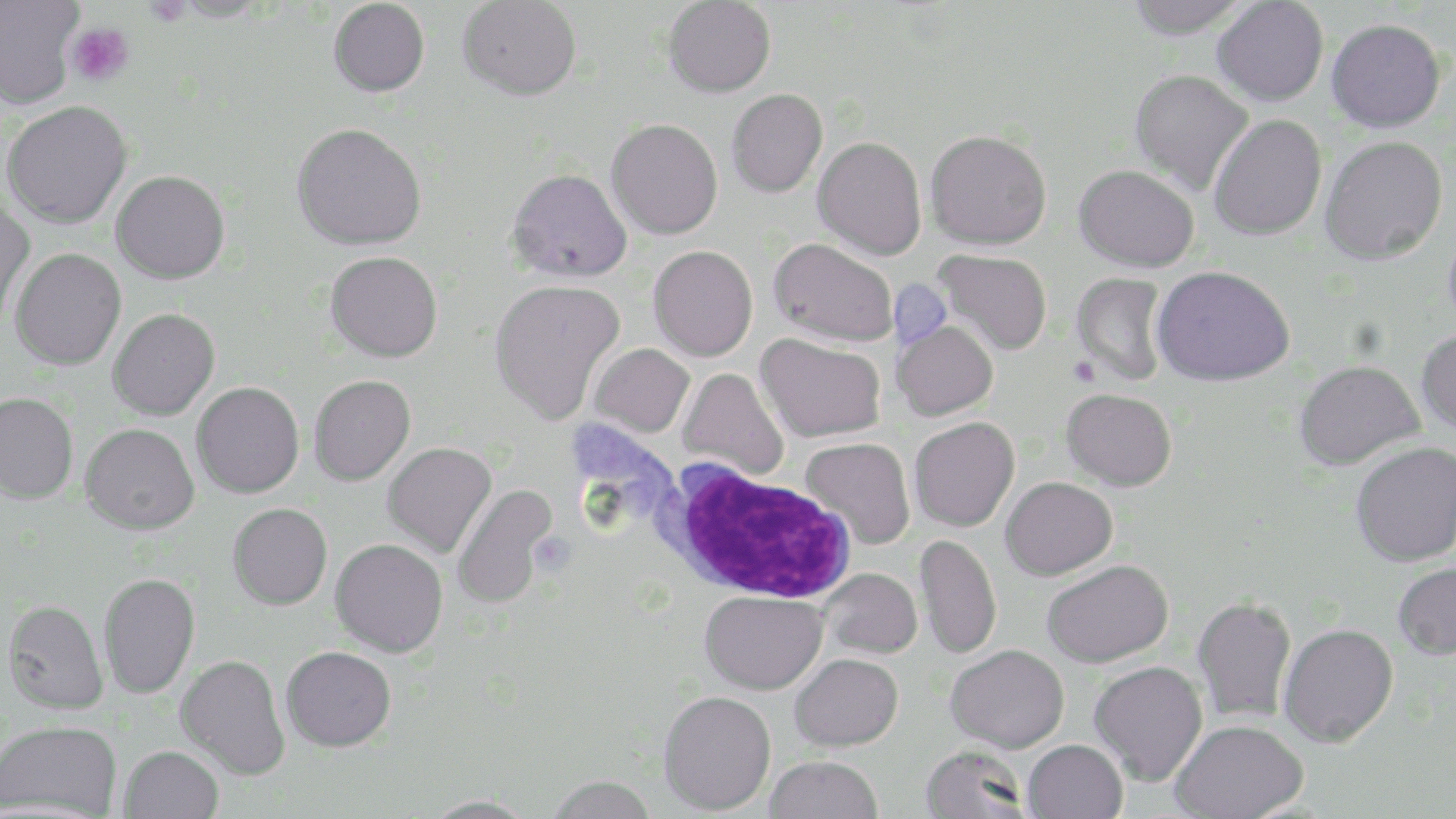
slide_level_diagnosis: Plasmodium falciparum
uninfected_red_blood_cell_locations: 'approximate bounding boxes as named x1/y1/x2/y2 corners in pixels: (x1=0, y1=0, x2=82, y2=109), (x1=167, y1=0, x2=274, y2=23), (x1=328, y1=0, x2=429, y2=97), (x1=458, y1=0, x2=581, y2=101), (x1=1125, y1=0, x2=1251, y2=39), (x1=663, y1=1, x2=776, y2=97), (x1=1212, y1=1, x2=1328, y2=106), (x1=1326, y1=18, x2=1445, y2=132), (x1=1130, y1=69, x2=1254, y2=195), (x1=726, y1=89, x2=827, y2=197), (x1=2, y1=101, x2=133, y2=228), (x1=1208, y1=114, x2=1327, y2=241), (x1=606, y1=118, x2=722, y2=239), (x1=291, y1=122, x2=426, y2=250), (x1=925, y1=129, x2=1052, y2=250), (x1=812, y1=136, x2=927, y2=260), (x1=1320, y1=136, x2=1448, y2=265), (x1=1074, y1=164, x2=1199, y2=272), (x1=507, y1=167, x2=632, y2=282), (x1=111, y1=170, x2=230, y2=284), (x1=0, y1=200, x2=35, y2=324), (x1=1443, y1=217, x2=1456, y2=337), (x1=769, y1=238, x2=897, y2=347), (x1=648, y1=245, x2=758, y2=361), (x1=10, y1=249, x2=126, y2=370), (x1=933, y1=249, x2=1052, y2=355), (x1=325, y1=251, x2=443, y2=362), (x1=1151, y1=265, x2=1295, y2=385), (x1=1070, y1=273, x2=1172, y2=386), (x1=489, y1=279, x2=625, y2=424), (x1=108, y1=308, x2=220, y2=420), (x1=892, y1=319, x2=998, y2=420), (x1=1417, y1=328, x2=1456, y2=435), (x1=756, y1=333, x2=886, y2=442), (x1=588, y1=343, x2=695, y2=437), (x1=1294, y1=360, x2=1424, y2=470), (x1=677, y1=368, x2=789, y2=481), (x1=309, y1=374, x2=415, y2=485), (x1=192, y1=381, x2=304, y2=498), (x1=1061, y1=388, x2=1177, y2=491), (x1=0, y1=392, x2=78, y2=504), (x1=909, y1=417, x2=1019, y2=531), (x1=80, y1=422, x2=199, y2=534), (x1=800, y1=437, x2=915, y2=548), (x1=382, y1=442, x2=497, y2=558), (x1=1351, y1=442, x2=1456, y2=567), (x1=1000, y1=476, x2=1117, y2=580), (x1=450, y1=484, x2=559, y2=609), (x1=228, y1=503, x2=332, y2=610), (x1=914, y1=534, x2=1002, y2=660), (x1=330, y1=538, x2=448, y2=657), (x1=1041, y1=560, x2=1173, y2=667), (x1=1392, y1=562, x2=1456, y2=660), (x1=819, y1=568, x2=922, y2=659), (x1=99, y1=573, x2=200, y2=698), (x1=699, y1=590, x2=827, y2=695), (x1=1192, y1=596, x2=1297, y2=724), (x1=3, y1=601, x2=108, y2=714), (x1=1278, y1=623, x2=1398, y2=747), (x1=945, y1=644, x2=1069, y2=753), (x1=281, y1=646, x2=396, y2=751), (x1=175, y1=654, x2=290, y2=779), (x1=789, y1=654, x2=903, y2=751), (x1=1089, y1=661, x2=1207, y2=785), (x1=658, y1=690, x2=776, y2=814), (x1=1171, y1=719, x2=1308, y2=819), (x1=0, y1=720, x2=121, y2=818), (x1=1022, y1=739, x2=1127, y2=818), (x1=920, y1=744, x2=1031, y2=818), (x1=120, y1=746, x2=223, y2=819), (x1=764, y1=755, x2=883, y2=818), (x1=544, y1=775, x2=659, y2=819), (x1=420, y1=795, x2=538, y2=819)'
field_of_view: one of a larger specimen
preparation: thin blood film
magnification: 1000x
modality: optical microscopy
stain: May-Grünwald-Giemsa
white_blood_cell_locations: 'approximate bounding boxes as named x1/y1/x2/y2 corners in pixels: (x1=657, y1=462, x2=859, y2=605)'
platelet_locations: 'approximate bounding boxes as named x1/y1/x2/y2 corners in pixels: (x1=144, y1=0, x2=192, y2=27), (x1=65, y1=23, x2=134, y2=86), (x1=894, y1=285, x2=946, y2=352), (x1=1070, y1=355, x2=1101, y2=387)'
image_size: 1456×819 pixels